Report the malaria status of this cell.
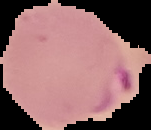
It is parasitized.

image type = segmented cell region with the area outside set to black
preparation = thin blood smear
image size = 151×130 pixels